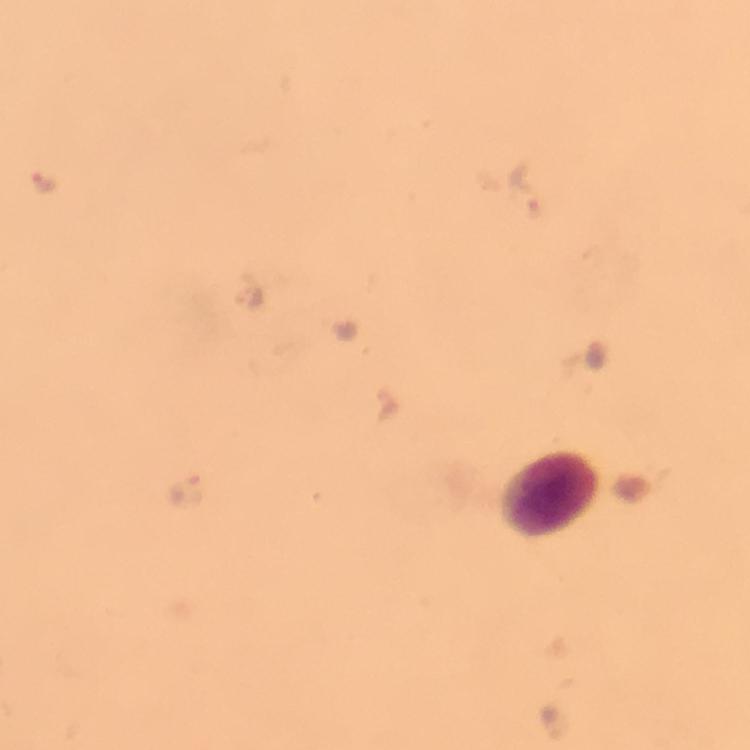
Approximate centers as (x, y) in pixels.
Summary:
  - Leukocyte locations: (546, 491)
  - Malaria parasite locations: (39, 178), (522, 187), (251, 297), (187, 489)
  - Magnification: 100x
  - Context: from a diagnostic examination for malaria
  - Cropped from: a single field of view
  - Preparation: thick blood smear
  - Immersion oil: used
  - Image size: 750×750 pixels
  - Capture: smartphone camera through the microscope
  - Stain: Giemsa